Locate every Plasmodium falciparum-infected red blood cell.
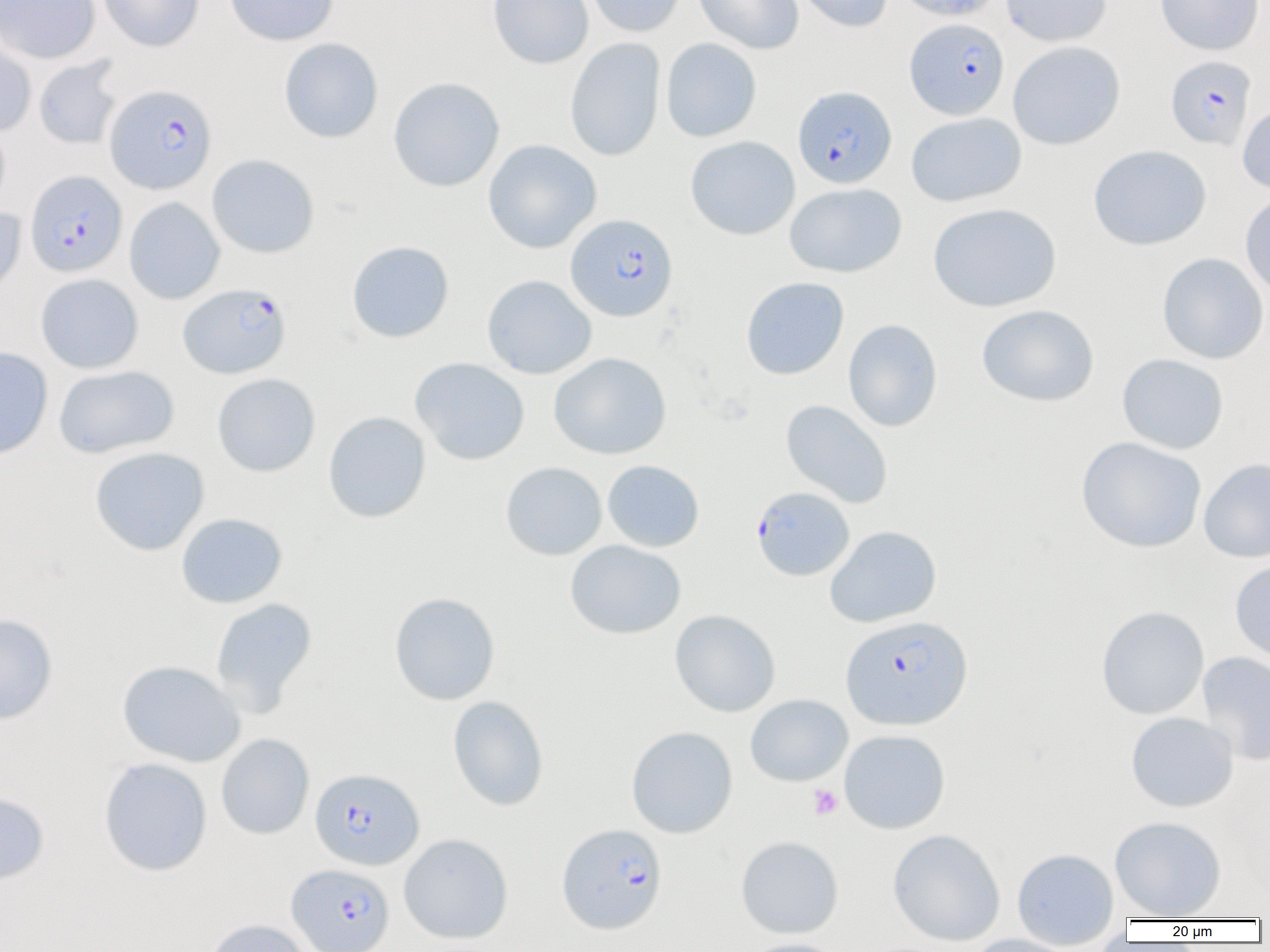
Approximate bounding boxes as named x1/y1/x2/y2 corners in pixels.
Plasmodium falciparum-infected red blood cells: (x1=904, y1=17, x2=1009, y2=119), (x1=1166, y1=55, x2=1256, y2=150), (x1=105, y1=84, x2=217, y2=194), (x1=793, y1=85, x2=897, y2=188), (x1=25, y1=170, x2=127, y2=277), (x1=566, y1=213, x2=678, y2=321), (x1=179, y1=283, x2=290, y2=378), (x1=751, y1=486, x2=854, y2=581), (x1=841, y1=616, x2=972, y2=730), (x1=311, y1=768, x2=423, y2=870), (x1=557, y1=823, x2=667, y2=933), (x1=287, y1=863, x2=395, y2=952).

Uninfected red blood cell locations: (x1=0, y1=0, x2=100, y2=64), (x1=98, y1=0, x2=204, y2=51), (x1=225, y1=0, x2=339, y2=46), (x1=487, y1=0, x2=594, y2=69), (x1=584, y1=0, x2=685, y2=37), (x1=694, y1=0, x2=804, y2=54), (x1=791, y1=0, x2=893, y2=33), (x1=893, y1=0, x2=1004, y2=21), (x1=1001, y1=0, x2=1111, y2=47), (x1=1155, y1=0, x2=1264, y2=55), (x1=0, y1=31, x2=37, y2=136), (x1=279, y1=38, x2=383, y2=143), (x1=565, y1=38, x2=665, y2=161), (x1=661, y1=38, x2=762, y2=142), (x1=1008, y1=41, x2=1125, y2=150), (x1=33, y1=56, x2=123, y2=150), (x1=388, y1=77, x2=505, y2=192), (x1=1237, y1=101, x2=1270, y2=194), (x1=906, y1=112, x2=1026, y2=207), (x1=0, y1=120, x2=11, y2=214), (x1=685, y1=136, x2=800, y2=240), (x1=483, y1=139, x2=601, y2=253), (x1=1088, y1=145, x2=1211, y2=250), (x1=207, y1=154, x2=319, y2=258), (x1=784, y1=183, x2=906, y2=278), (x1=1240, y1=191, x2=1270, y2=298), (x1=124, y1=197, x2=224, y2=304), (x1=928, y1=203, x2=1062, y2=312), (x1=0, y1=207, x2=27, y2=302), (x1=346, y1=240, x2=454, y2=343), (x1=1157, y1=252, x2=1269, y2=364), (x1=35, y1=273, x2=143, y2=374), (x1=481, y1=275, x2=597, y2=379), (x1=740, y1=277, x2=849, y2=379), (x1=976, y1=304, x2=1099, y2=407), (x1=843, y1=319, x2=943, y2=432), (x1=0, y1=347, x2=53, y2=459), (x1=549, y1=352, x2=671, y2=459), (x1=1117, y1=353, x2=1229, y2=454), (x1=410, y1=357, x2=530, y2=465), (x1=53, y1=365, x2=179, y2=458), (x1=212, y1=373, x2=320, y2=477), (x1=780, y1=400, x2=893, y2=509), (x1=323, y1=411, x2=431, y2=523), (x1=1076, y1=436, x2=1207, y2=553), (x1=89, y1=447, x2=210, y2=555), (x1=1199, y1=458, x2=1270, y2=563), (x1=602, y1=460, x2=704, y2=552), (x1=500, y1=461, x2=607, y2=560), (x1=176, y1=513, x2=288, y2=608), (x1=825, y1=525, x2=942, y2=628), (x1=565, y1=540, x2=686, y2=639), (x1=1229, y1=558, x2=1270, y2=665), (x1=389, y1=592, x2=501, y2=706), (x1=210, y1=598, x2=317, y2=715), (x1=1096, y1=606, x2=1209, y2=719), (x1=670, y1=609, x2=781, y2=717), (x1=0, y1=613, x2=58, y2=725), (x1=1197, y1=651, x2=1270, y2=766), (x1=117, y1=660, x2=245, y2=767), (x1=745, y1=694, x2=853, y2=786), (x1=447, y1=695, x2=549, y2=811), (x1=1125, y1=712, x2=1239, y2=812), (x1=627, y1=726, x2=738, y2=838), (x1=839, y1=729, x2=950, y2=833), (x1=216, y1=734, x2=314, y2=839), (x1=98, y1=757, x2=212, y2=876), (x1=0, y1=792, x2=49, y2=886), (x1=1110, y1=815, x2=1227, y2=919), (x1=887, y1=829, x2=1006, y2=946), (x1=399, y1=833, x2=513, y2=943), (x1=736, y1=836, x2=844, y2=939), (x1=1011, y1=848, x2=1119, y2=948), (x1=203, y1=919, x2=314, y2=952), (x1=963, y1=934, x2=1082, y2=952), (x1=740, y1=938, x2=850, y2=952). Platelet locations: (x1=807, y1=784, x2=843, y2=819). Slide-level diagnosis: Plasmodium falciparum. Image is 1270×952 pixels. 1000x magnification. Light microscopy. Single field of view. Thin blood film.